Classify this cell by malaria status.
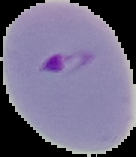

Parasitized.

{
  "image_size": "136×157 pixels",
  "image_type": "segmented cell region with the area outside set to black",
  "preparation": "thin blood film"
}